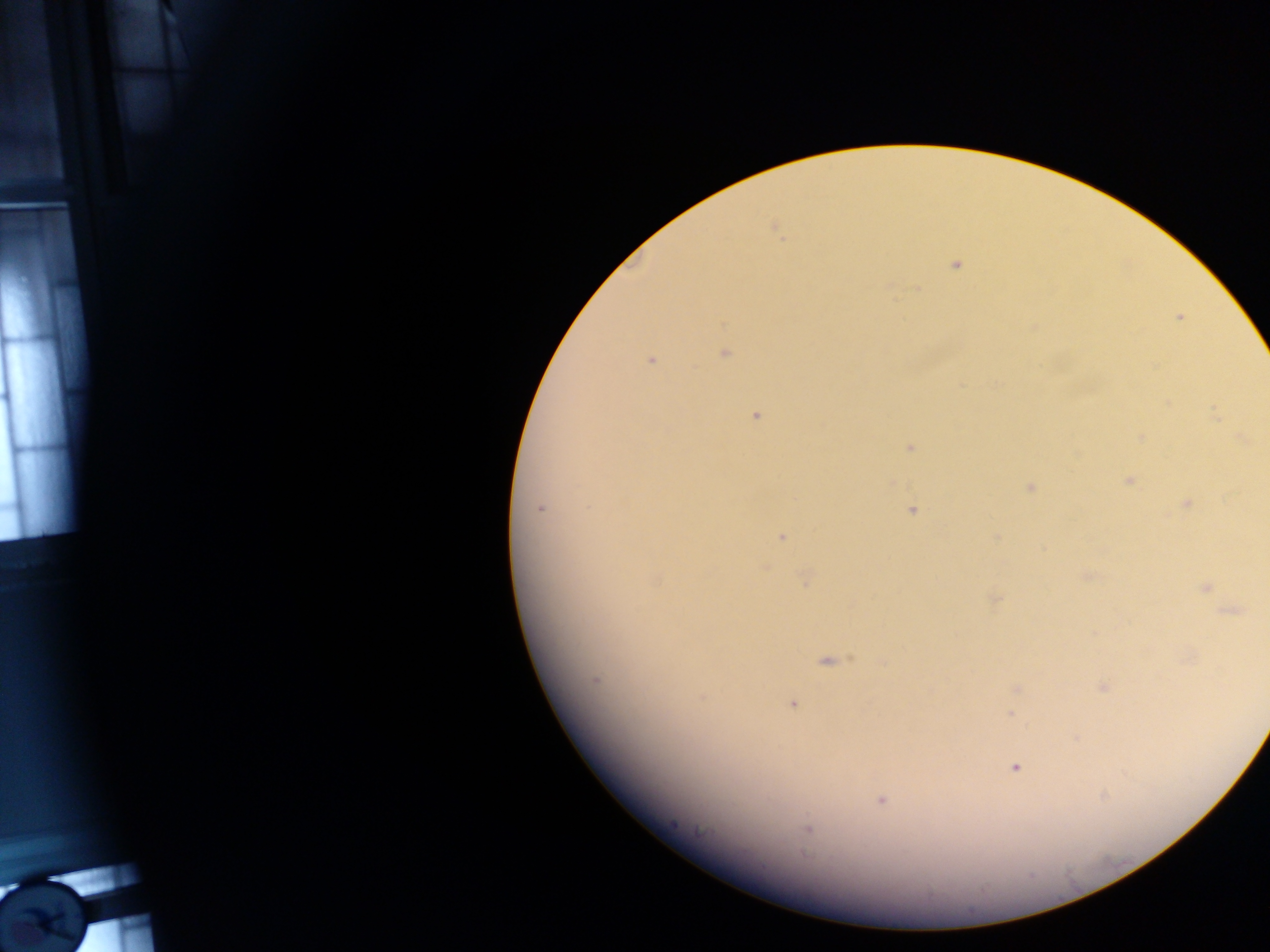
Approximate centers as x y in pixels. Malaria parasite locations: 775 228; 955 265; 1178 317; 1033 327; 724 352; 650 359; 1167 404; 755 414; 1215 416; 1141 437; 1242 438; 909 447; 1129 480; 890 483; 1029 486; 1186 502; 539 508; 912 510; 781 536; 996 537; 764 567; 1085 576; 805 578; 1205 587; 994 598; 1230 610; 826 660; 882 661; 595 679; 1102 687; 1016 690; 702 695; 792 703; 1011 712; 1014 767; 881 799; 807 829. Image is 1270×952 pixels. One field of view. Collected in Ghana. Thick blood film. Photographed through a microscope with a mobile-phone camera.